Look for parasitized red blood cells.
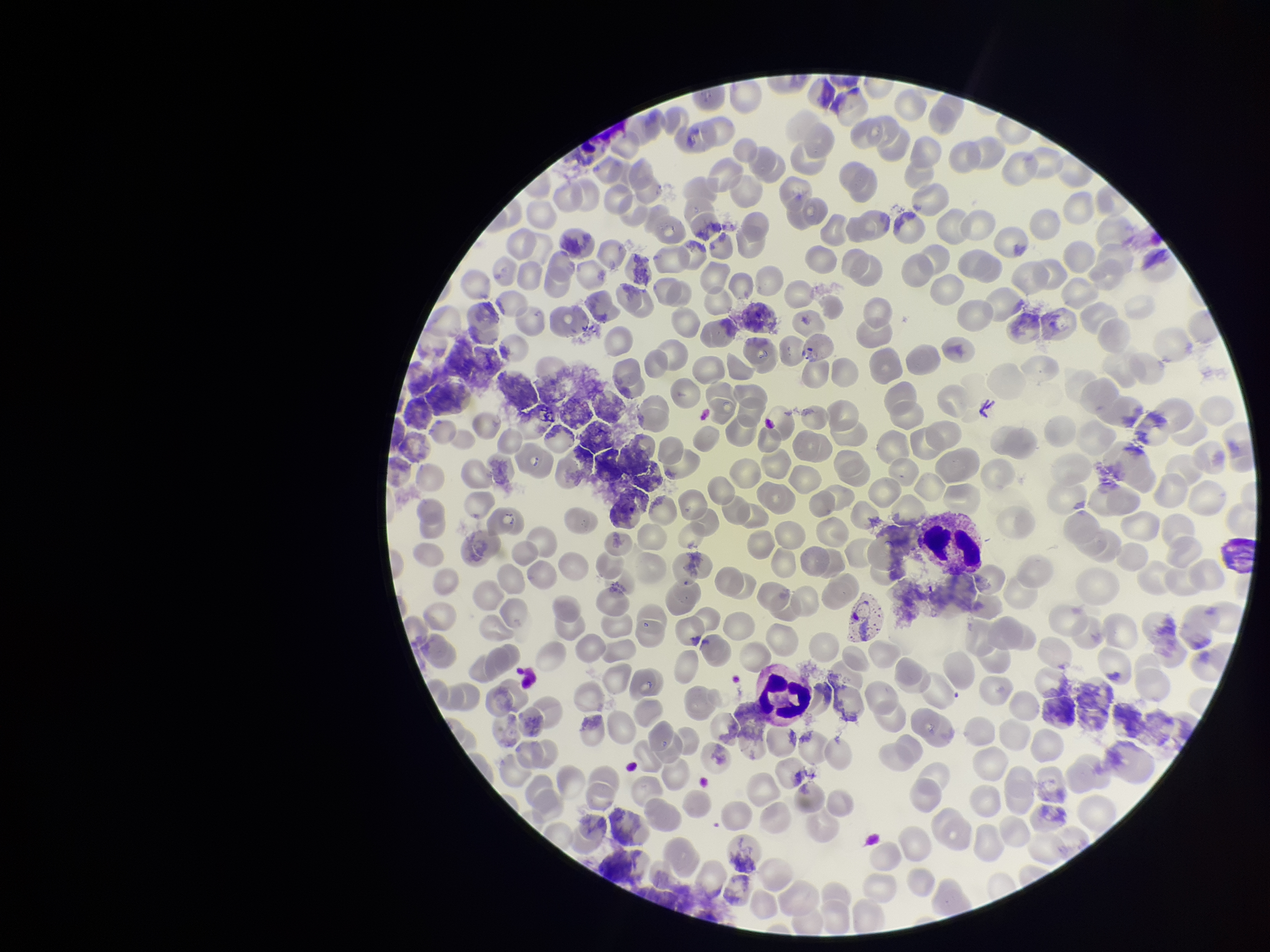
None identified.

{
  "red_blood_cell_count": 154,
  "parasitized_red_blood_cell_count": 0,
  "field_of_view": "single",
  "image_size": "1270×952 pixels",
  "capture": "smartphone photograph through the microscope eyepiece",
  "preparation": "thin blood smear",
  "stain": "Giemsa",
  "patient_malaria_status": "infected",
  "species_reported_for_this_patient": "Plasmodium vivax"
}